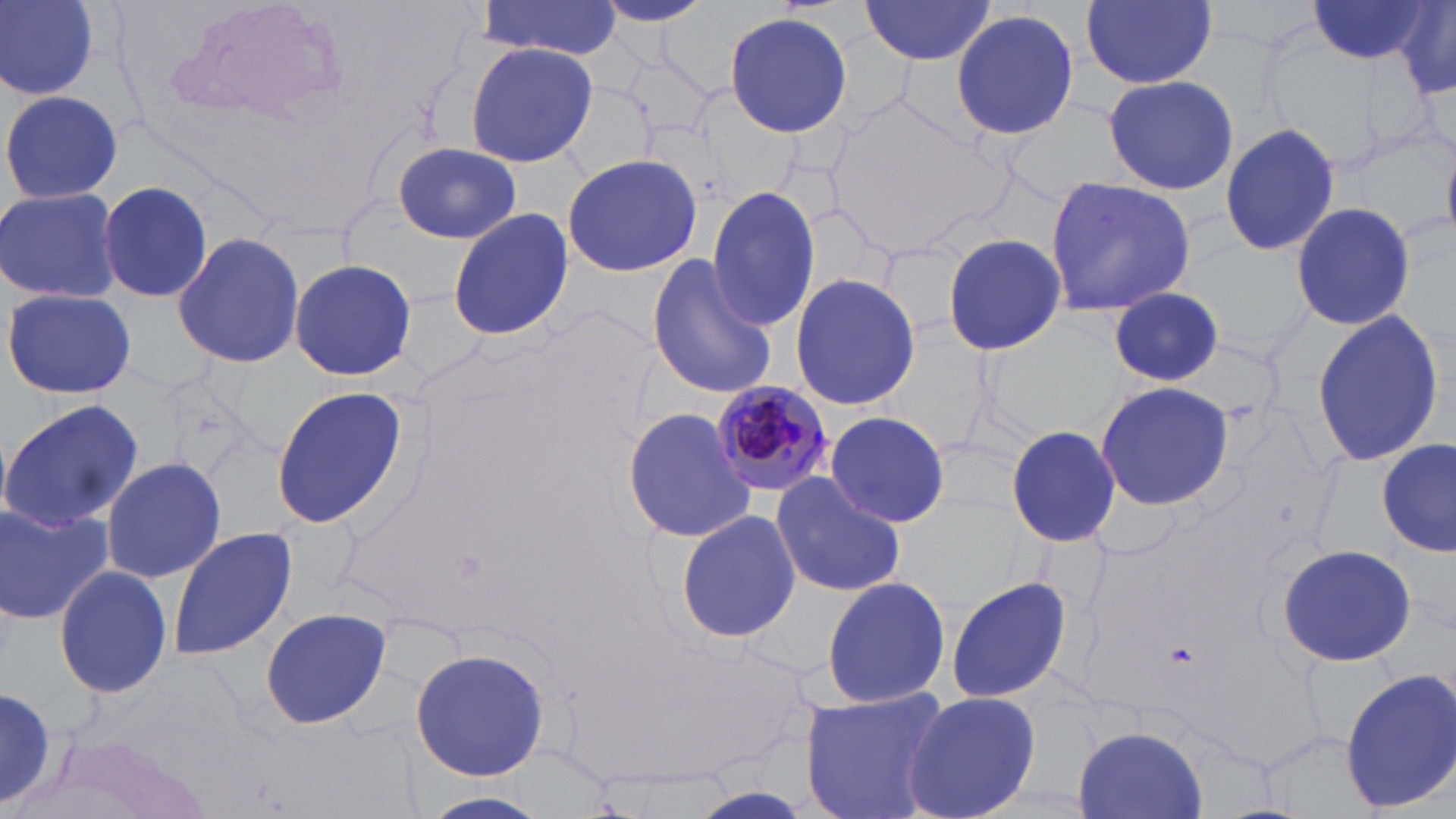
Approximate bounding boxes as (x1,y1)-(x2,y2) corner pairs in pixels. Plasmodium malariae-infected red blood cell locations: (716,383)-(833,499). Uninfected red blood cell locations: (2,0)-(100,98), (589,0)-(718,26), (1083,0)-(1217,89), (1304,0)-(1435,65), (858,1)-(996,65), (1388,1)-(1456,94), (478,2)-(623,59), (950,10)-(1079,140), (724,11)-(853,137), (465,43)-(598,168), (1101,74)-(1239,196), (2,89)-(123,205), (1219,122)-(1341,259), (390,142)-(528,244), (561,153)-(702,278), (1043,177)-(1198,317), (99,179)-(215,305), (706,185)-(821,331), (0,186)-(124,305), (1288,202)-(1416,333), (446,206)-(574,342), (173,230)-(304,369), (942,233)-(1065,357), (645,252)-(779,401), (289,257)-(421,381), (789,271)-(921,411), (4,288)-(137,400), (1109,288)-(1223,385), (1311,309)-(1447,468), (268,383)-(407,529), (1094,384)-(1234,508), (0,399)-(144,531), (622,407)-(753,543), (826,411)-(950,529), (1005,423)-(1121,549), (1377,439)-(1453,557), (102,456)-(226,583), (771,473)-(906,597), (0,502)-(113,626), (674,508)-(802,645), (166,525)-(297,660), (1277,543)-(1417,667), (54,565)-(173,700), (819,573)-(950,711), (945,575)-(1074,705), (258,606)-(393,729), (410,646)-(550,781), (1340,668)-(1456,813), (800,687)-(951,819), (0,688)-(60,808), (902,690)-(1041,819), (1070,725)-(1207,819). Slide-level diagnosis: Plasmodium malariae. Light microscopy. May-Grünwald-Giemsa stain. Single field of view. Thin blood smear. 1000x magnification. Image is 1456×819 pixels.